Locate every blood parasite and identify its species.
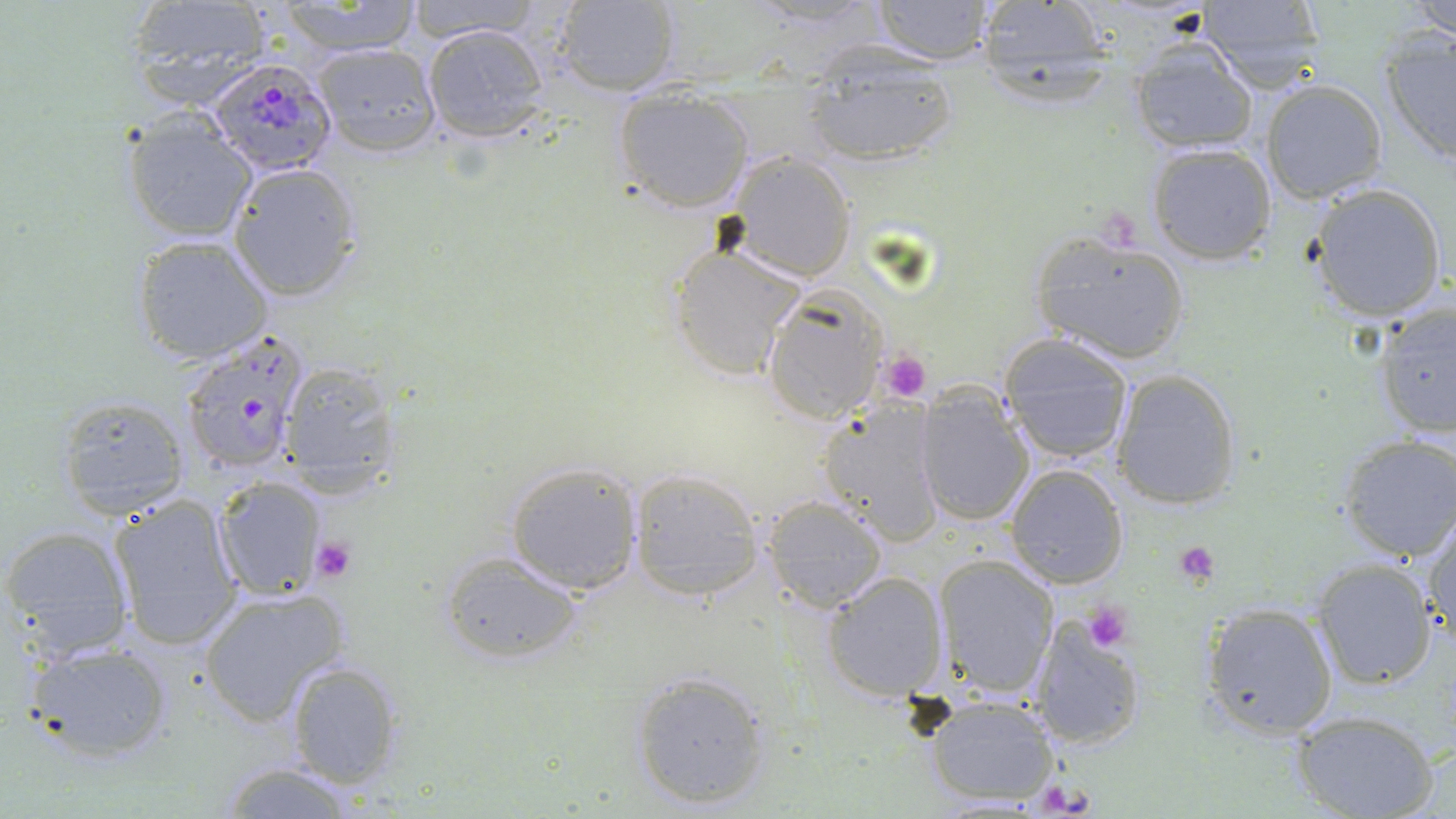

Approximate bounding boxes as (x1, y1, x2, y2) in pixels.
Plasmodium falciparum-infected red blood cells: (204, 56, 337, 175), (176, 334, 312, 479).
No Plasmodium ovale, Plasmodium malariae, Plasmodium vivax, Babesia divergens, or Trypanosoma brucei observed.

{
  "slide_level_diagnosis": "Plasmodium falciparum",
  "platelet_locations": "approximate bounding boxes as (x1, y1, x2, y2) in pixels: (1095, 214, 1142, 254), (876, 351, 932, 402), (310, 536, 356, 582), (1173, 541, 1220, 586), (1082, 599, 1135, 651)",
  "uninfected_red_blood_cell_locations": "approximate bounding boxes as (x1, y1, x2, y2) in pixels: (272, 0, 429, 56), (397, 0, 549, 44), (1410, 0, 1456, 39), (549, 1, 680, 95), (865, 1, 997, 64), (1195, 1, 1329, 90), (122, 2, 269, 110), (972, 2, 1117, 90), (421, 22, 552, 141), (1377, 29, 1456, 168), (1128, 44, 1258, 155), (312, 45, 441, 157), (800, 54, 960, 165), (1261, 79, 1388, 205), (611, 86, 753, 214), (120, 113, 257, 241), (1147, 142, 1278, 266), (726, 152, 856, 283), (228, 162, 363, 301), (1307, 183, 1449, 321), (1028, 230, 1192, 367), (130, 235, 274, 366), (668, 243, 804, 377), (761, 288, 887, 425), (1372, 304, 1456, 441), (999, 335, 1137, 467), (274, 364, 403, 496), (1110, 368, 1242, 511), (914, 388, 1036, 527), (54, 395, 190, 519), (818, 402, 947, 547), (1338, 434, 1456, 561), (505, 461, 641, 593), (1004, 462, 1128, 590), (627, 467, 767, 602), (213, 475, 328, 600), (107, 492, 243, 650), (762, 497, 888, 611), (1424, 511, 1456, 646), (1, 524, 135, 659), (438, 551, 583, 664), (934, 554, 1059, 697), (1311, 560, 1437, 689), (822, 571, 950, 703), (197, 587, 350, 724), (1200, 601, 1338, 739), (1031, 618, 1148, 751), (26, 641, 177, 763), (283, 658, 406, 789), (628, 670, 774, 811), (922, 694, 1063, 806), (1295, 712, 1438, 819), (212, 761, 368, 817)",
  "preparation": "thin blood smear",
  "stain": "May-Grünwald-Giemsa",
  "modality": "light microscopy",
  "magnification": "1000x",
  "image_size": "1456×819 pixels",
  "field_of_view": "one of a larger specimen"
}